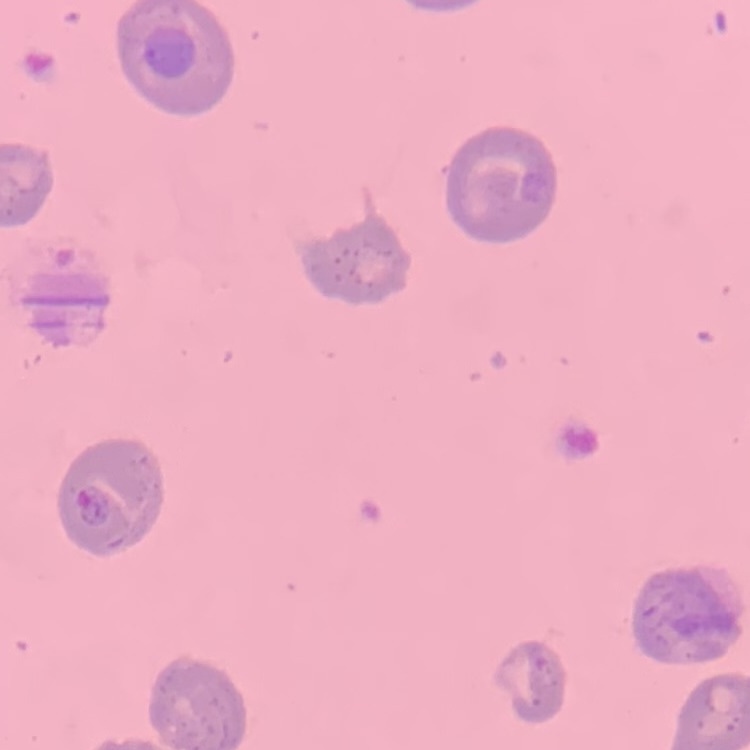 The erythrocytes exhibit no rouleaux formation. Square crop of a larger photomicrograph. Field's or Giemsa stain. Thin blood film.